Report the malaria status of this cell.
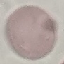
It is uninfected.

{
  "image_type": "cell patch, automatically extracted from a larger field of view and resized to 64 × 64 pixels",
  "capture": "smartphone through the microscope eyepiece",
  "preparation": "thin blood smear",
  "stain": "Giemsa"
}